Report the malaria status of this cell.
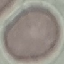

Uninfected.

Summary:
  - Capture: smartphone through the microscope eyepiece
  - Stain: Giemsa
  - Preparation: thin blood film
  - Image type: cell patch, automatically extracted from a larger field of view and resized to 64 × 64 pixels